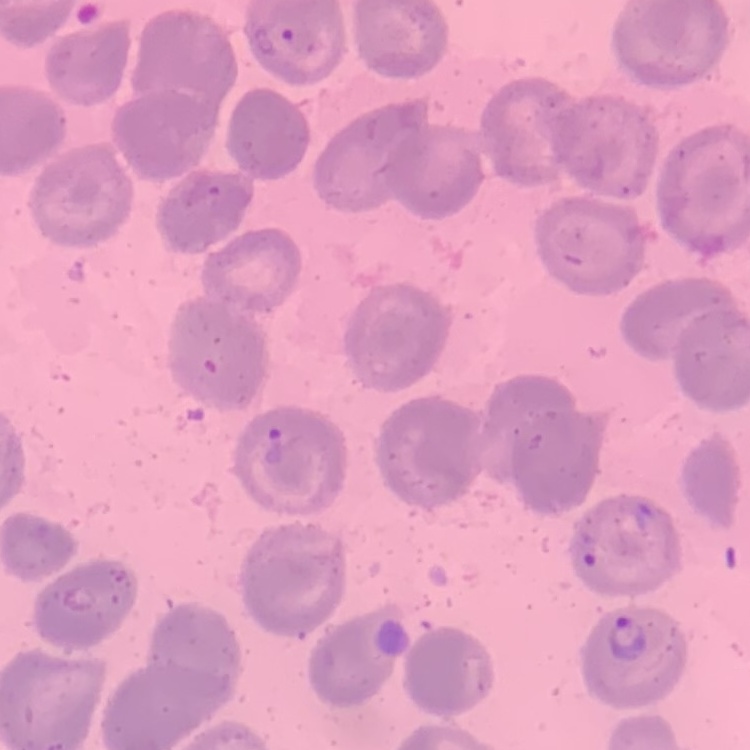

Summary:
  - Red blood cell morphology: no rouleaux formation
  - Stain: Field's or Giemsa
  - Image type: square crop of a larger photomicrograph
  - Preparation: thin peripheral smear